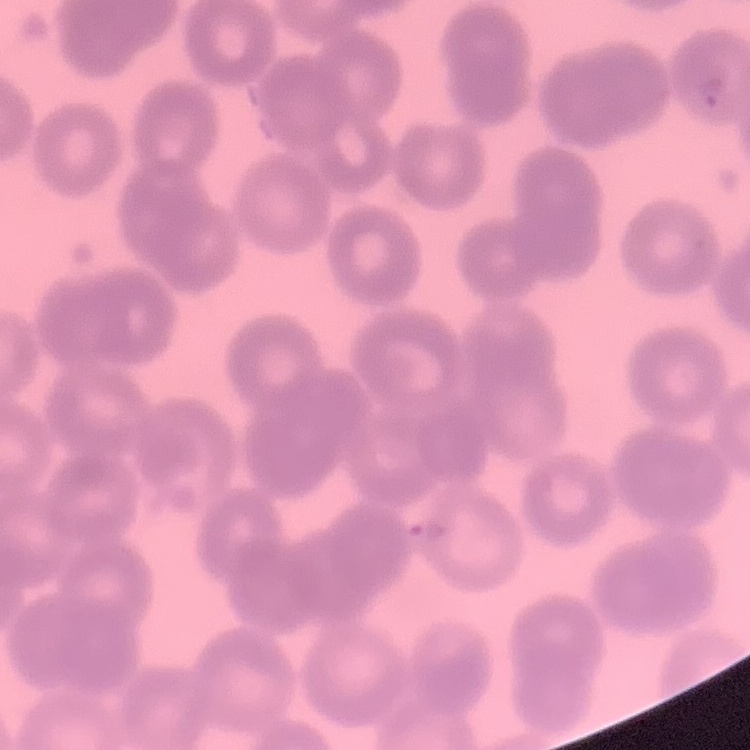 The erythrocytes show no rouleaux formation. Square crop of a larger photomicrograph. Field's or Giemsa stain. Thin peripheral smear.